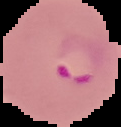 Image is 121×127 pixels. Malaria status: parasitized. From a thin blood smear. Cell region segmented out of the field of view; the surrounding area is masked to black.